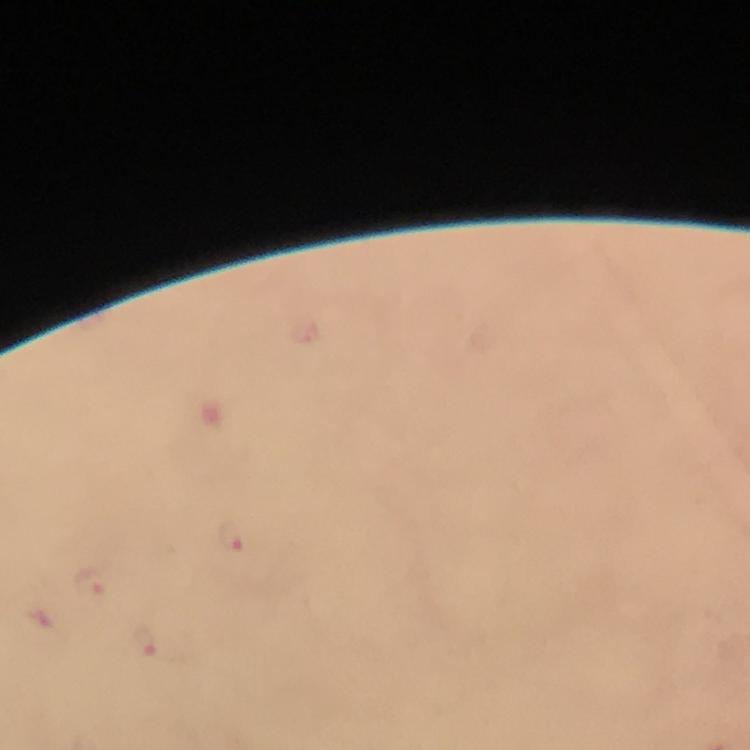
immersion_oil: used
plasmodium_parasite_locations: 'approximate centers as [x, y] in pixels: [229, 537], [89, 583], [148, 644]'
image_size: 750×750 pixels
stain: Giemsa
context: from a malaria diagnostic workup
preparation: thick blood smear
cropped_from: one field of view
capture: smartphone camera through the microscope
magnification: 100x